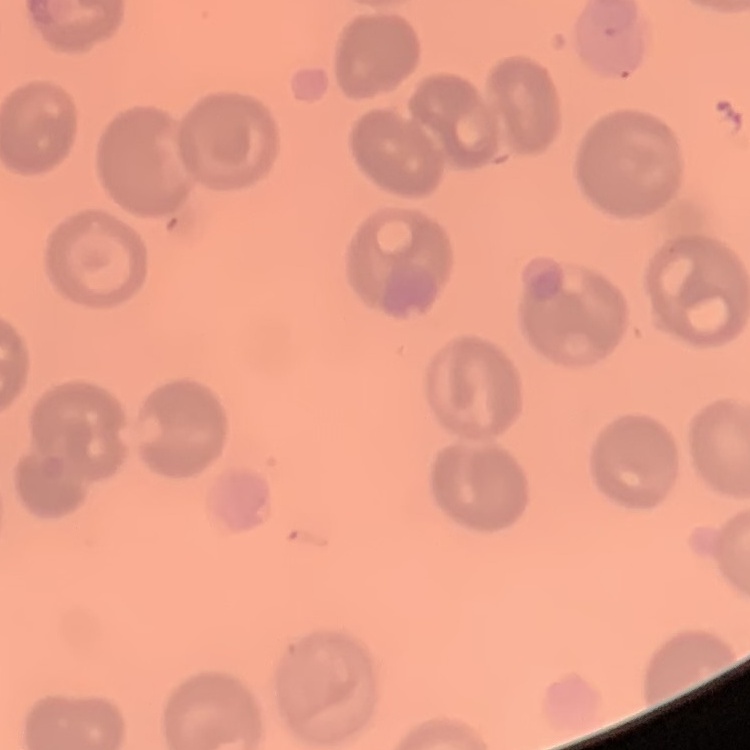
erythrocyte_morphology: no rouleaux formation
image_type: one tile cut from a larger photomicrograph
stain: Field's or Giemsa
preparation: thin blood film